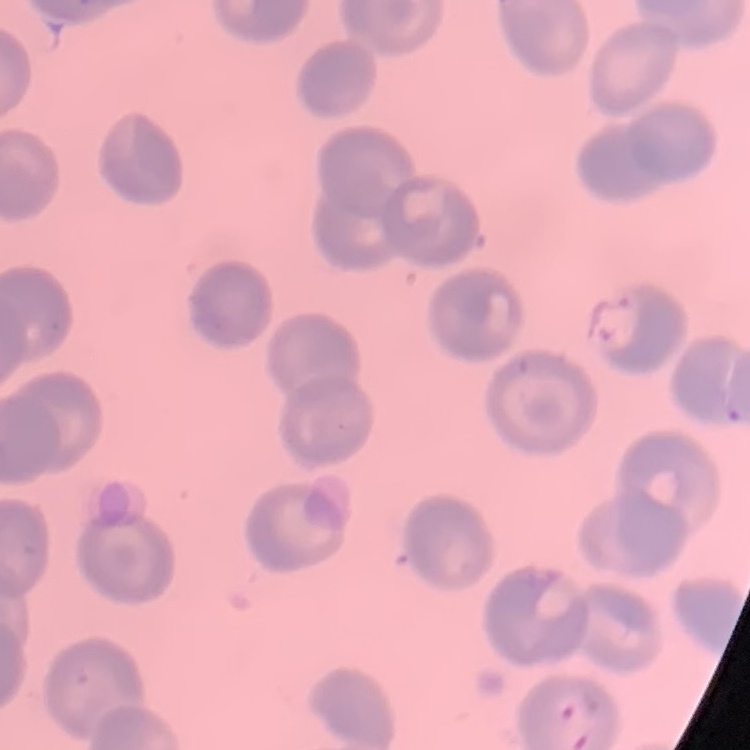
red blood cell morphology = no rouleaux formation
stain = Field's or Giemsa
image type = one tile cut from a larger photomicrograph
preparation = thin blood film